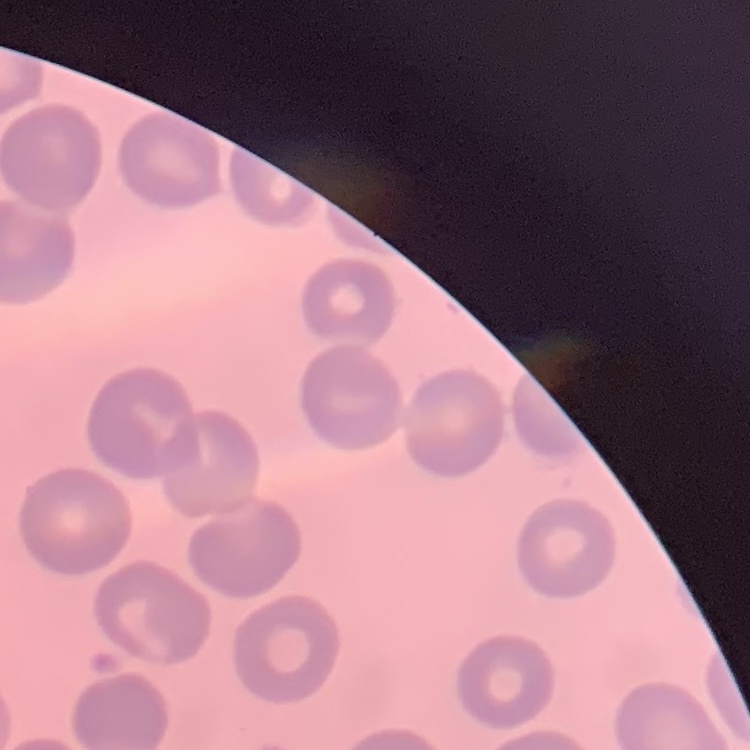

red blood cell morphology = no rouleaux formation
preparation = thin blood film
image type = square crop of a larger photomicrograph
stain = Field's or Giemsa